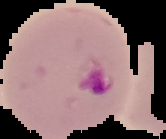
result = Plasmodium parasites detected
image size = 166×139 pixels
preparation = thin blood smear
image type = segmented cell region with the area outside set to black